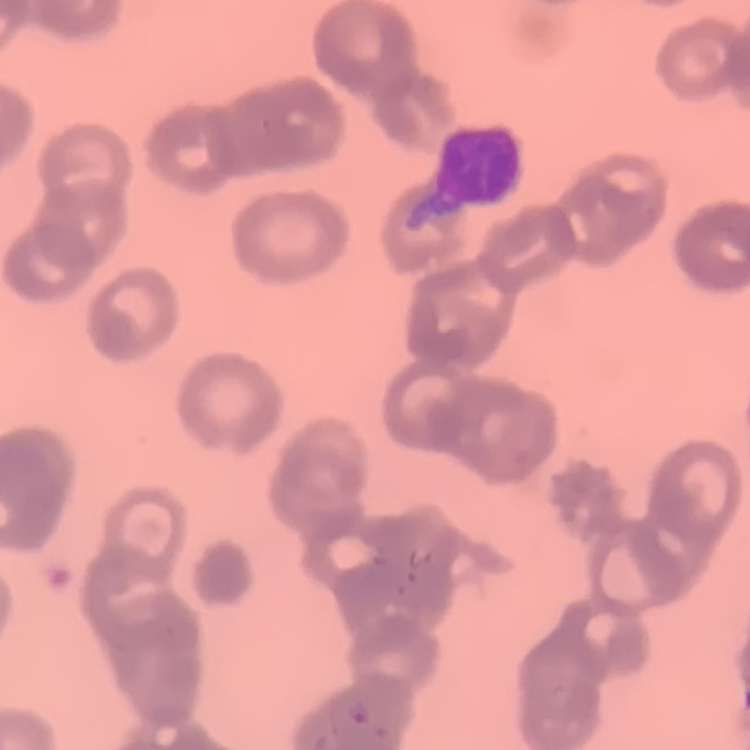 The erythrocytes exhibit rouleaux formation. Thin peripheral smear. Field's or Giemsa stain. Square crop of a larger photomicrograph.